Classify this cell by malaria status.
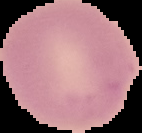

It is uninfected.

image type = segmented cell region on a black background
image size = 142×133 pixels
preparation = thin blood smear